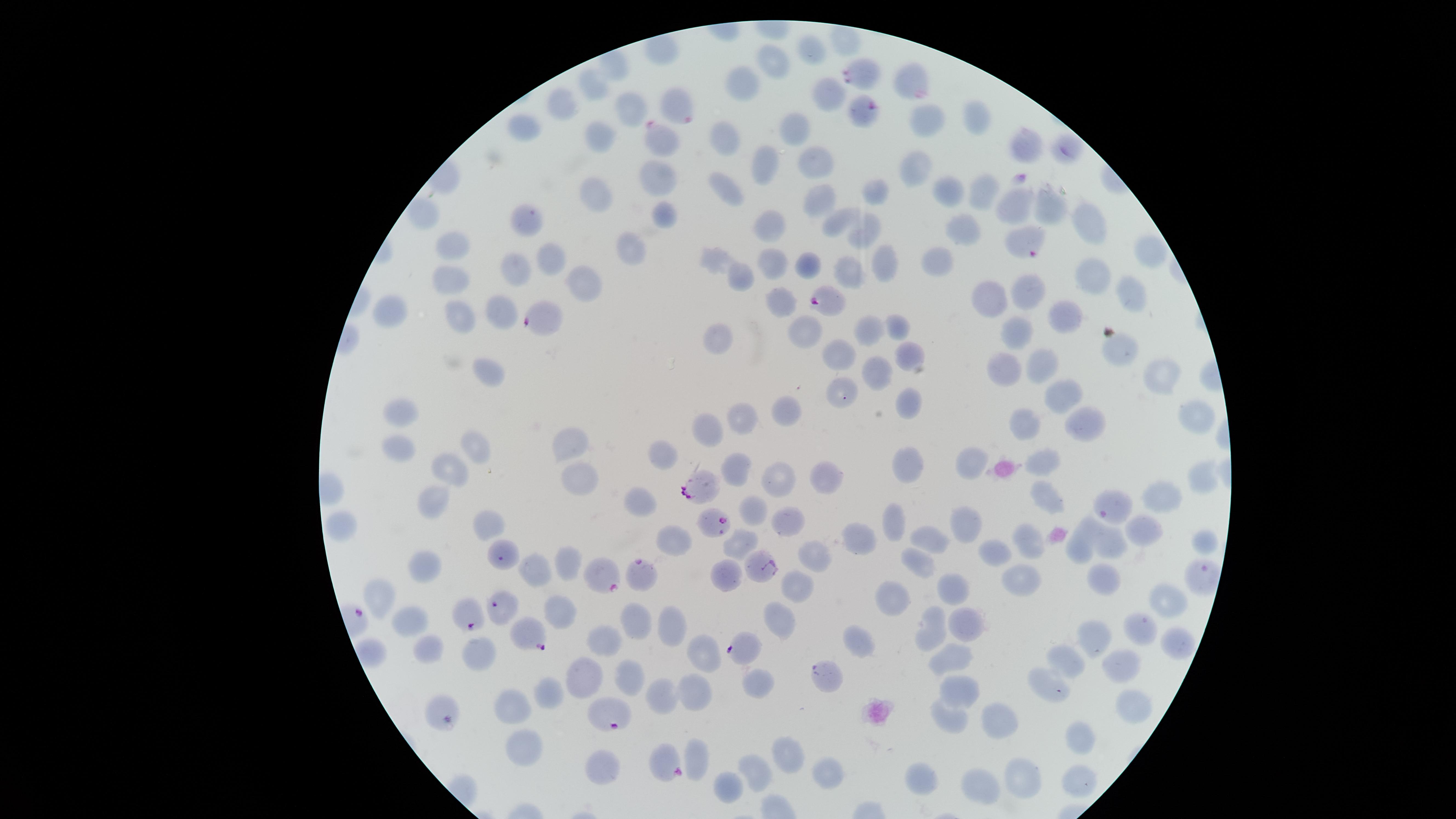

field of view = single
uninfected red blood cells = approximate marker points as {x, y} in pixels: {809, 53}, {773, 65}, {913, 74}, {594, 86}, {741, 88}, {824, 96}, {630, 103}, {560, 109}, {926, 119}, {978, 119}, {795, 126}, {530, 128}, {603, 139}, {726, 142}, {1027, 144}, {915, 158}, {808, 160}, {763, 162}, {657, 174}, {985, 189}, {728, 191}, {873, 192}, {947, 192}, {597, 193}, {819, 200}, {1017, 201}, {1049, 202}, {666, 209}, {1087, 216}, {844, 218}, {526, 221}, {774, 224}, {867, 226}, {963, 231}, {452, 245}, {633, 246}, {1148, 249}, {548, 252}, {715, 256}, {885, 263}, {770, 265}, {807, 265}, {852, 271}, {1090, 273}, {508, 274}, {743, 276}, {589, 281}, {451, 283}, {1032, 291}, {1133, 291}, {993, 297}, {786, 303}, {501, 312}, {390, 315}, {1057, 315}, {460, 317}, {896, 327}, {1019, 332}, {807, 333}, {868, 333}, {716, 338}, {1117, 349}, {835, 354}, {903, 354}, {1040, 368}, {1002, 369}, {491, 372}, {876, 374}, {1158, 374}, {842, 389}, {1068, 397}, {903, 400}, {789, 410}, {1191, 411}, {407, 418}, {747, 418}, {1026, 423}, {1091, 423}, {712, 426}, {400, 440}, {473, 442}, {572, 447}, {659, 454}, {970, 459}, {1042, 462}, {738, 463}, {910, 465}, {452, 468}, {774, 475}, {1203, 479}, {576, 480}, {820, 480}, {1163, 497}, {1043, 499}, {1117, 499}, {435, 500}, {640, 505}, {753, 513}, {965, 523}, {490, 524}, {788, 524}, {898, 524}, {1141, 532}, {862, 538}, {1027, 540}, {932, 541}, {677, 543}, {740, 544}, {1084, 545}, {1114, 545}, {998, 553}, {813, 556}, {919, 564}, {570, 567}, {427, 568}, {542, 570}, {723, 572}, {801, 574}, {1024, 576}, {1103, 581}, {950, 586}, {387, 597}, {1163, 599}, {895, 602}, {786, 618}, {559, 619}, {636, 619}, {407, 622}, {962, 625}, {1140, 625}, {670, 628}, {939, 631}, {608, 637}, {1097, 639}, {1177, 641}, {861, 642}, {430, 652}, {481, 655}, {704, 655}, {954, 655}, {1071, 657}, {1125, 664}, {589, 671}, {631, 675}, {1051, 681}, {756, 683}, {963, 690}, {665, 693}, {697, 693}, {551, 694}, {441, 708}, {511, 709}, {1131, 710}, {1007, 720}, {951, 723}, {1081, 739}, {525, 748}, {696, 754}, {786, 755}, {665, 762}, {826, 766}, {605, 768}, {754, 771}, {1022, 777}, {921, 781}, {1077, 783}, {983, 785}, {723, 786}
image size = 1456×819 pixels
capture = smartphone photograph through the microscope eyepiece
stain = Giemsa
species = Plasmodium falciparum
parasitized red blood cells = approximate marker points as {x, y} in pixels: {866, 73}, {866, 114}, {661, 142}, {1064, 153}, {825, 299}, {702, 491}, {712, 520}, {761, 569}, {641, 573}, {601, 577}, {468, 615}, {526, 633}
visible region = circular
preparation = thin smear of blood
presence = malaria parasites detected